Locate every Plasmodium vivax-infected red blood cell.
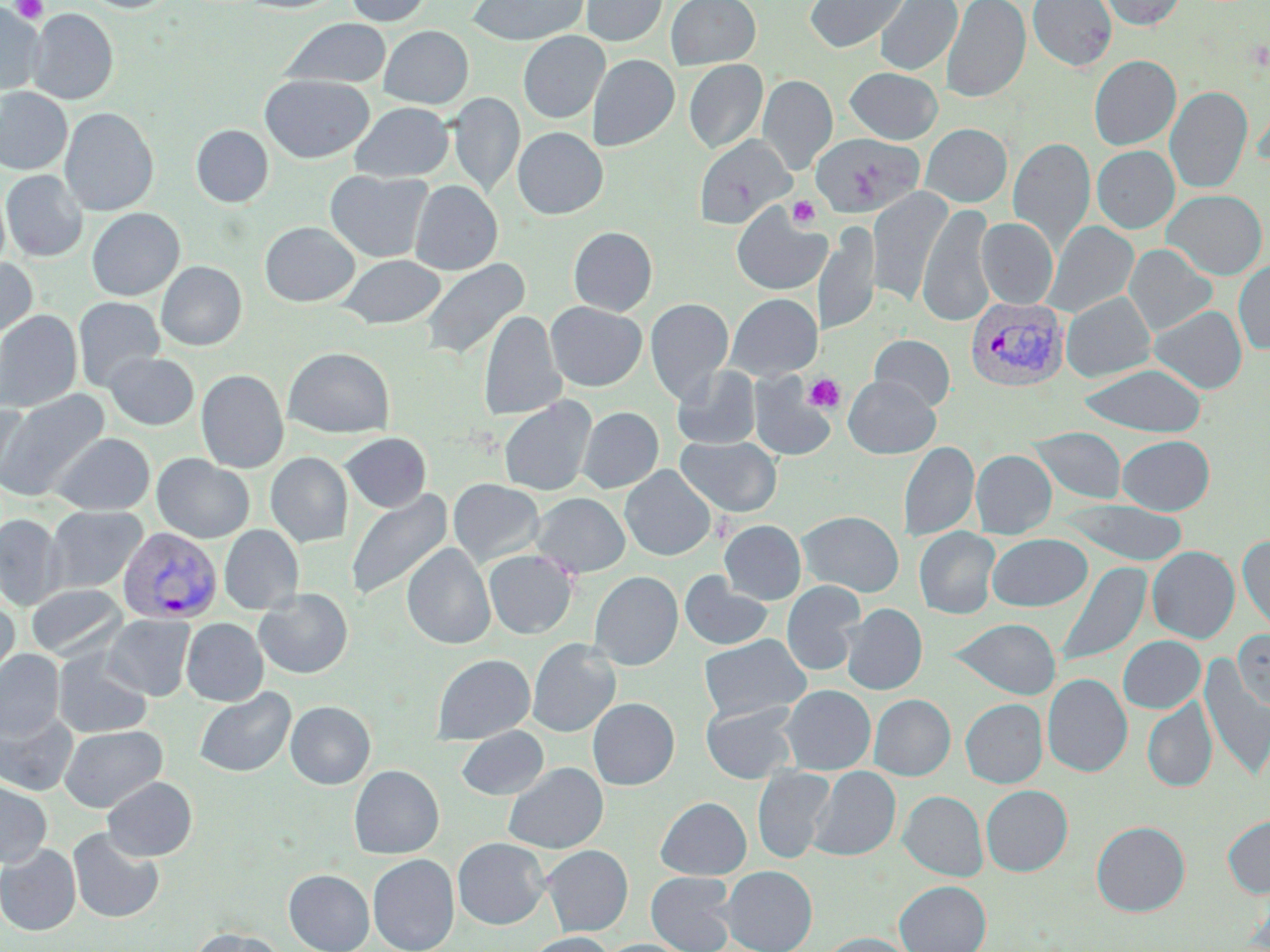
Approximate bounding boxes as (x1, y1, x2, y2) in pixels.
Plasmodium vivax-infected red blood cells: (965, 296, 1069, 391), (116, 527, 223, 624).

slide-level diagnosis = Plasmodium vivax
modality = light microscopy
uninfected red blood cell locations = approximate bounding boxes as (x1, y1, x2, y2) in pixels: (81, 0, 177, 13), (240, 0, 343, 13), (345, 0, 431, 26), (467, 0, 589, 45), (581, 0, 667, 46), (665, 0, 761, 69), (804, 0, 911, 53), (874, 0, 961, 76), (941, 0, 1030, 103), (1028, 0, 1116, 70), (1097, 0, 1185, 30), (0, 4, 43, 95), (27, 9, 118, 104), (280, 18, 392, 89), (379, 25, 473, 109), (518, 31, 609, 123), (587, 54, 679, 151), (1089, 55, 1181, 150), (684, 60, 767, 153), (846, 67, 942, 143), (260, 74, 374, 163), (758, 74, 837, 174), (1165, 86, 1253, 193), (0, 88, 72, 175), (448, 92, 524, 197), (1253, 92, 1270, 171), (350, 102, 454, 182), (59, 107, 158, 215), (920, 123, 1012, 207), (191, 125, 273, 207), (513, 127, 608, 219), (811, 133, 924, 217), (693, 135, 793, 228), (1008, 137, 1095, 251), (1092, 145, 1179, 233), (1, 170, 87, 262), (326, 170, 433, 263), (410, 180, 502, 275), (867, 188, 953, 306), (1163, 189, 1267, 279), (731, 203, 831, 296), (918, 203, 996, 326), (87, 208, 185, 300), (976, 217, 1058, 308), (1043, 221, 1139, 318), (260, 222, 359, 307), (814, 222, 880, 336), (568, 226, 657, 315), (1124, 244, 1217, 336), (338, 254, 445, 329), (0, 255, 36, 340), (419, 258, 529, 362), (1233, 259, 1270, 354), (156, 261, 247, 350), (1061, 291, 1155, 382), (726, 293, 822, 381), (73, 296, 165, 392), (645, 298, 734, 404), (546, 301, 646, 391), (1149, 305, 1247, 393), (0, 310, 83, 412), (478, 310, 566, 421), (870, 334, 954, 411), (284, 347, 394, 438), (104, 351, 199, 430), (1078, 363, 1207, 436), (672, 365, 762, 450), (196, 369, 289, 473), (750, 374, 836, 462), (843, 375, 940, 458), (0, 390, 109, 502), (499, 397, 595, 496), (0, 398, 31, 491), (578, 406, 663, 493), (1030, 427, 1126, 504), (341, 432, 431, 512), (52, 433, 155, 515), (676, 435, 781, 517), (1117, 435, 1214, 515), (899, 441, 979, 542), (971, 450, 1056, 538), (266, 452, 352, 547), (152, 454, 254, 543), (620, 466, 716, 560), (448, 479, 544, 567), (346, 488, 452, 602), (532, 493, 630, 578), (1060, 500, 1188, 565), (45, 505, 147, 593), (798, 510, 904, 597), (0, 514, 64, 610), (719, 520, 805, 604), (219, 525, 304, 615), (914, 527, 1000, 619), (987, 533, 1092, 611), (1237, 535, 1270, 637), (401, 543, 495, 649), (1147, 546, 1240, 643), (484, 549, 577, 639), (1055, 562, 1151, 669), (1052, 565, 1141, 776), (590, 571, 683, 670), (679, 572, 774, 651), (782, 581, 865, 675), (26, 584, 127, 660), (254, 588, 353, 679), (0, 600, 19, 692), (841, 604, 927, 695), (102, 615, 195, 700), (181, 618, 268, 706), (951, 618, 1061, 699), (1234, 630, 1270, 713), (699, 634, 809, 721), (1118, 636, 1205, 713), (527, 638, 621, 737), (0, 648, 65, 738), (53, 649, 153, 738), (431, 653, 535, 744), (1199, 660, 1270, 782), (1043, 673, 1132, 777), (781, 685, 875, 774), (194, 687, 296, 777), (869, 694, 955, 780), (588, 697, 679, 789), (961, 698, 1047, 788), (1142, 699, 1217, 792), (285, 700, 375, 789), (701, 702, 798, 783), (0, 707, 78, 796), (59, 724, 167, 812), (456, 726, 548, 800), (504, 762, 607, 853), (349, 765, 444, 858), (753, 766, 835, 863), (809, 767, 900, 860), (102, 776, 197, 860), (0, 780, 51, 868), (981, 785, 1073, 876), (899, 790, 987, 881), (656, 797, 751, 879), (1222, 815, 1270, 898), (1091, 821, 1190, 916), (67, 827, 164, 923), (453, 837, 549, 929), (0, 844, 81, 935), (542, 845, 632, 935), (368, 854, 459, 952), (721, 866, 817, 952), (284, 869, 374, 952), (646, 872, 737, 952), (895, 880, 991, 952), (188, 928, 287, 952), (524, 932, 615, 952), (819, 933, 914, 952), (599, 939, 692, 952)
field of view = single
preparation = thin blood film
stain = May-Grünwald-Giemsa
magnification = 1000x
image size = 1270×952 pixels
platelet locations = approximate bounding boxes as (x1, y1, x2, y2) in pixels: (11, 0, 48, 24), (788, 196, 820, 229), (804, 374, 846, 413), (711, 513, 734, 542)